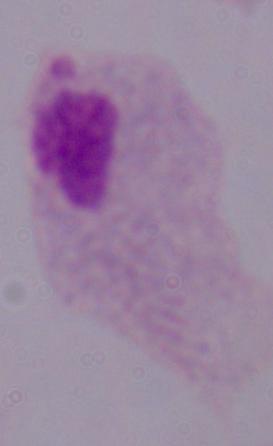
Captured at 1000x magnification. Photomicrograph. A trichomonad is seen.